Give the position of every malaria parasite.
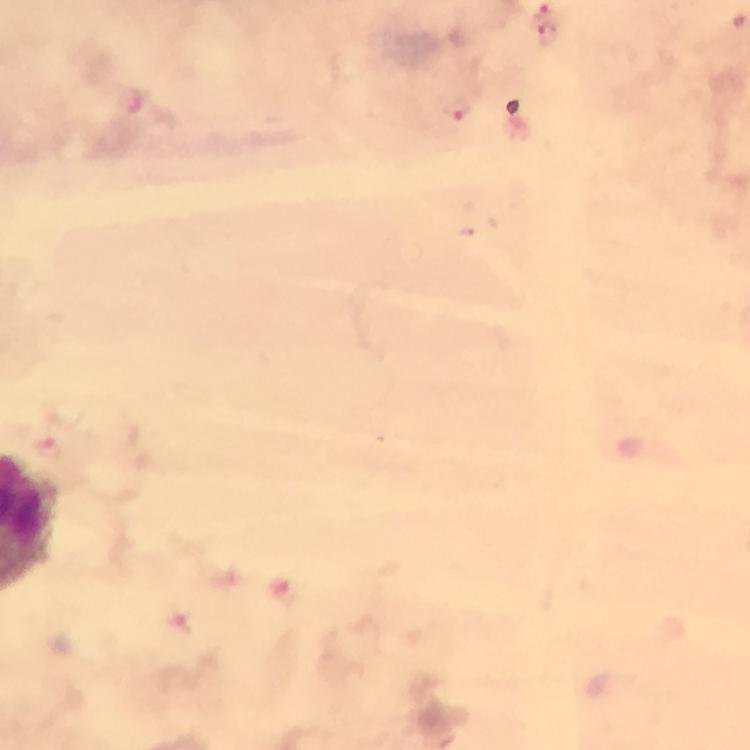

Approximate centers as [x, y] in pixels.
Malaria parasites: [549, 39], [458, 110], [47, 450], [177, 620].

Summary:
  - Stain: Giemsa
  - Immersion oil: used
  - Preparation: thick blood film
  - Cropped from: a single field of view
  - Magnification: 100x
  - Image size: 750×750 pixels
  - Capture: smartphone camera through the microscope
  - Context: from a malaria diagnostic workup